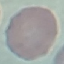

malaria_status: uninfected
image_type: cell patch, automatically extracted from a larger field of view and resized to 64 × 64 pixels
stain: Giemsa
capture: smartphone through the microscope eyepiece
preparation: thin blood smear